Point out malaria parasites and leukocytes.
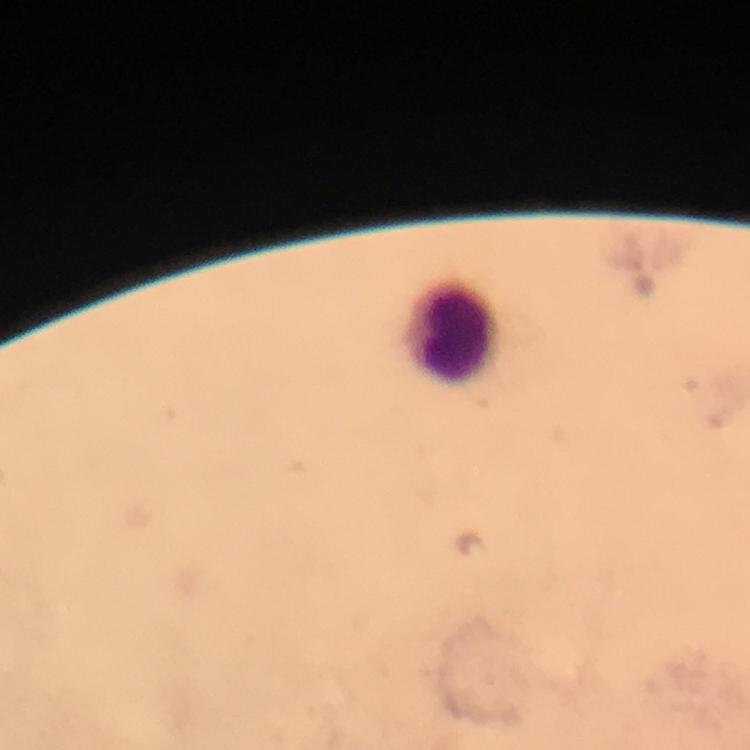
No malaria parasites seen.
Approximate centers as {x, y} in pixels.
Leukocytes: {455, 328}.

cropped_from: a single field of view
context: from a diagnostic examination for malaria
capture: smartphone photograph through a microscope
preparation: thick blood smear
image_size: 750×750 pixels
immersion_oil: used
magnification: 100x
stain: Giemsa